Identify the parasite.
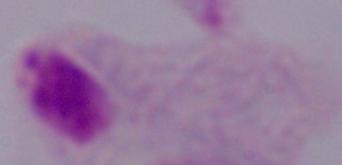
A trichomonad.

Photomicrograph. Captured at 1000x magnification.